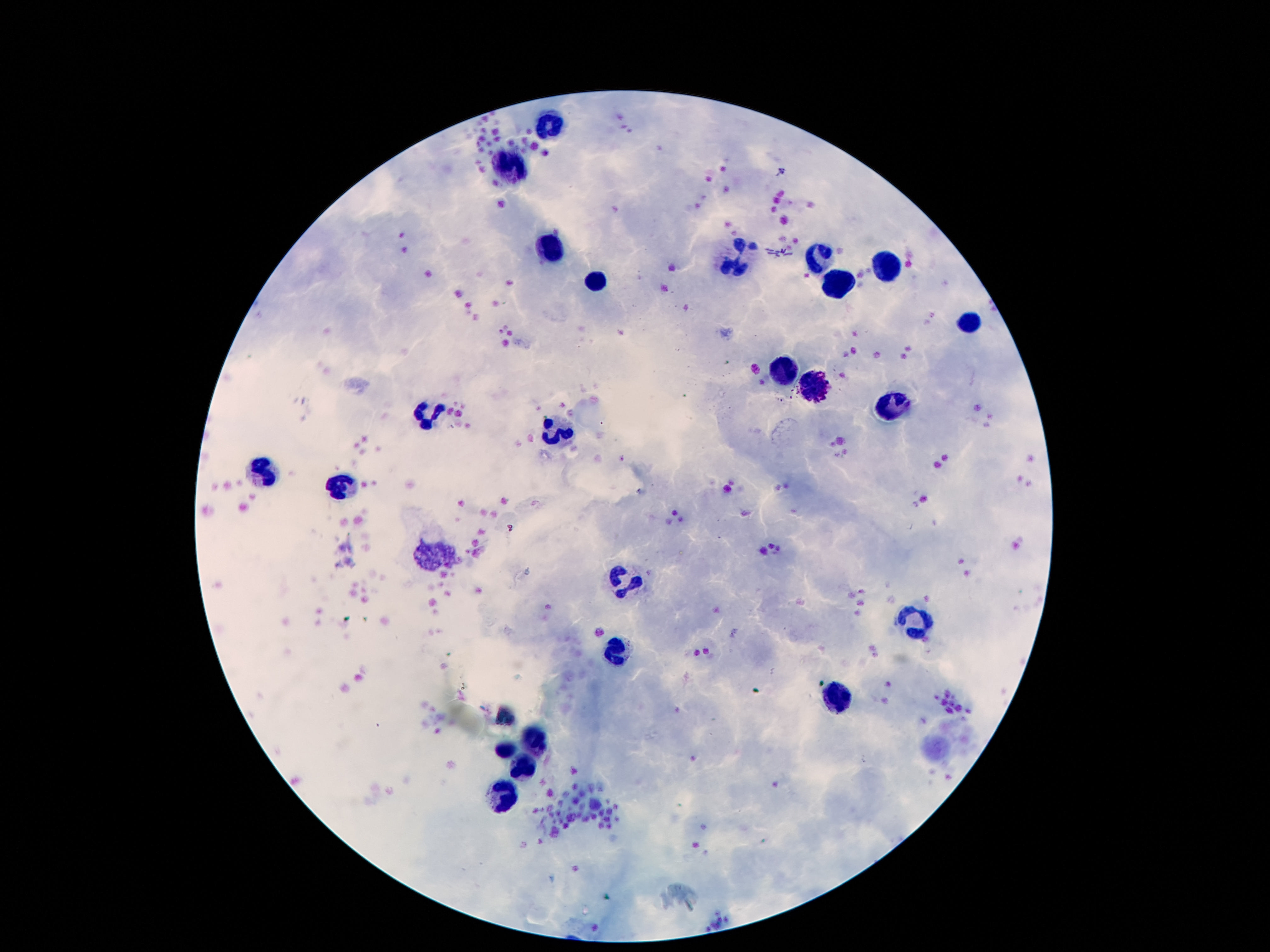
Approximate centers as (x, y) in pixels. Leukocyte locations: (554, 124), (512, 170), (550, 246), (821, 256), (737, 260), (888, 268), (835, 282), (590, 284), (970, 317), (783, 372), (817, 385), (896, 410), (434, 416), (556, 433), (262, 473), (342, 489), (435, 553), (628, 581), (911, 616), (621, 654), (838, 697), (504, 715), (537, 739), (508, 751), (529, 765), (506, 790). Smartphone photograph taken through the microscope eyepiece. 100x magnification. Patient malaria status: uninfected. Giemsa-stained preparation. Image is 1270×952 pixels. One field from this slide. Thick blood smear.